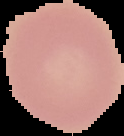
Image is 124×136 pixels. Result: no Plasmodium parasites seen. Segmented cell region on a black background. From a thin blood smear.